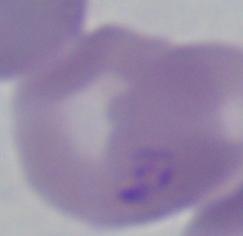

A Babesia parasite is shown. Photomicrograph. Captured at 1000x magnification.